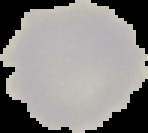 From a thin blood film. Segmented cell region on a black background. Image is 148×133 pixels. Result: negative for Plasmodium parasites.